Point out leukocytes.
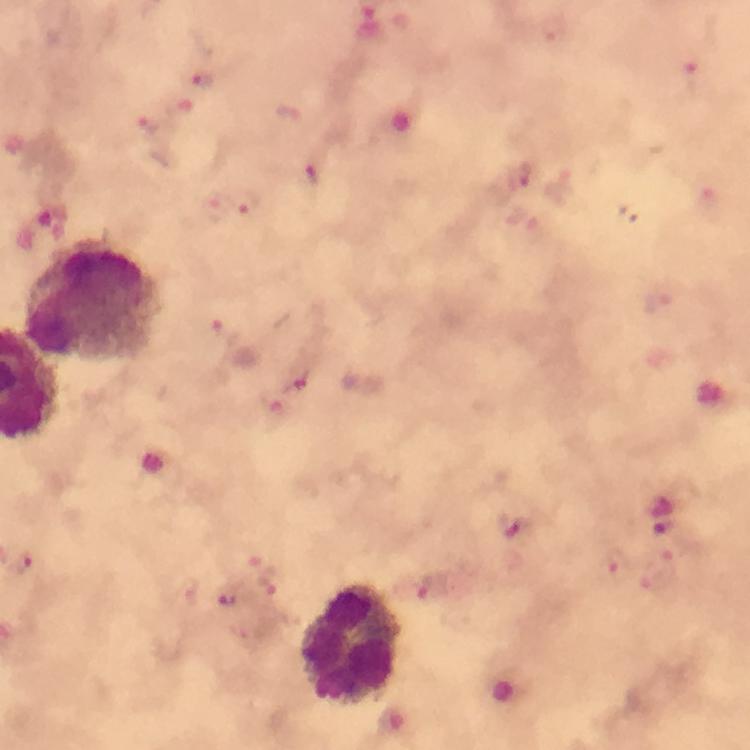

Approximate centers as {x, y} in pixels.
Leukocytes: {92, 300}, {351, 640}.

Plasmodium parasite locations: {553, 34}, {201, 78}, {147, 124}, {310, 175}, {517, 176}, {244, 204}, {226, 331}, {287, 367}, {271, 402}, {514, 524}, {20, 562}, {261, 564}, {617, 564}, {265, 583}, {432, 587}, {225, 598}. Cropped region of a single field of view. Image is 750×750 pixels. Giemsa stain. From a malaria diagnostic workup. Immersion oil was used. Thick blood smear. 100x magnification. Smartphone photograph taken through a microscope.